Assess this cell for malaria.
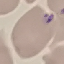

Uninfected.

image type = automatically extracted cell patch, resized to 64 × 64 pixels
stain = Giemsa
capture = smartphone through the microscope eyepiece
preparation = thin blood film